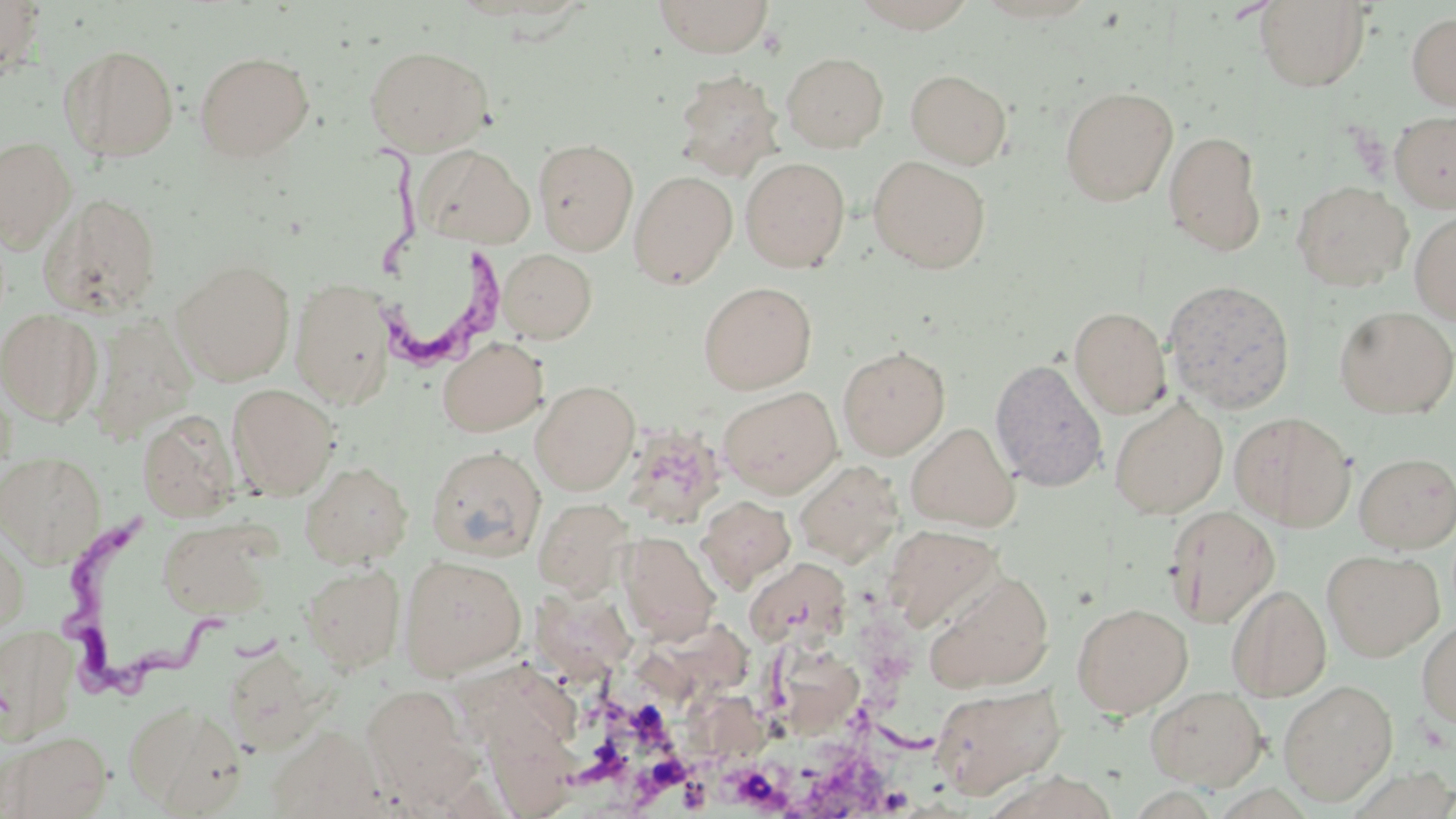
Summary:
  - Coordinate format: approximate bounding boxes as named x1/y1/x2/y2 corners in pixels
  - Uninfected red blood cell locations: (x1=0, y1=0, x2=45, y2=80), (x1=653, y1=0, x2=774, y2=58), (x1=853, y1=0, x2=978, y2=32), (x1=1254, y1=1, x2=1371, y2=92), (x1=1406, y1=11, x2=1456, y2=112), (x1=60, y1=44, x2=180, y2=162), (x1=365, y1=45, x2=493, y2=156), (x1=194, y1=51, x2=314, y2=162), (x1=782, y1=52, x2=888, y2=152), (x1=905, y1=69, x2=1012, y2=169), (x1=673, y1=70, x2=783, y2=181), (x1=1060, y1=86, x2=1178, y2=206), (x1=1389, y1=109, x2=1456, y2=213), (x1=1163, y1=130, x2=1266, y2=255), (x1=0, y1=136, x2=76, y2=251), (x1=532, y1=137, x2=639, y2=255), (x1=414, y1=144, x2=536, y2=249), (x1=868, y1=155, x2=991, y2=273), (x1=740, y1=157, x2=850, y2=272), (x1=629, y1=170, x2=738, y2=288), (x1=1291, y1=180, x2=1413, y2=291), (x1=39, y1=192, x2=164, y2=318), (x1=1410, y1=211, x2=1456, y2=325), (x1=497, y1=248, x2=597, y2=342), (x1=172, y1=260, x2=295, y2=385), (x1=290, y1=278, x2=395, y2=408), (x1=1162, y1=279, x2=1296, y2=413), (x1=698, y1=281, x2=817, y2=393), (x1=1069, y1=306, x2=1172, y2=419), (x1=1333, y1=306, x2=1456, y2=418), (x1=0, y1=308, x2=102, y2=425), (x1=88, y1=312, x2=198, y2=443), (x1=438, y1=337, x2=547, y2=437), (x1=837, y1=345, x2=951, y2=460), (x1=989, y1=358, x2=1107, y2=491), (x1=530, y1=380, x2=640, y2=495), (x1=227, y1=384, x2=339, y2=499), (x1=719, y1=386, x2=842, y2=499), (x1=1110, y1=398, x2=1228, y2=519), (x1=137, y1=410, x2=239, y2=522), (x1=1229, y1=411, x2=1356, y2=531), (x1=622, y1=421, x2=728, y2=530), (x1=906, y1=422, x2=1019, y2=531), (x1=426, y1=446, x2=546, y2=562), (x1=0, y1=452, x2=106, y2=567), (x1=1355, y1=452, x2=1456, y2=552), (x1=794, y1=459, x2=904, y2=566), (x1=301, y1=462, x2=412, y2=568), (x1=696, y1=496, x2=796, y2=591), (x1=532, y1=498, x2=633, y2=598), (x1=1165, y1=505, x2=1281, y2=628), (x1=158, y1=520, x2=274, y2=619), (x1=883, y1=524, x2=1005, y2=632), (x1=0, y1=526, x2=30, y2=638), (x1=618, y1=531, x2=720, y2=643), (x1=1322, y1=548, x2=1443, y2=661), (x1=399, y1=555, x2=527, y2=679), (x1=744, y1=557, x2=851, y2=650), (x1=300, y1=563, x2=406, y2=673), (x1=924, y1=570, x2=1056, y2=693), (x1=1227, y1=584, x2=1331, y2=702), (x1=530, y1=588, x2=642, y2=694), (x1=1071, y1=602, x2=1192, y2=718), (x1=1416, y1=618, x2=1456, y2=727), (x1=0, y1=624, x2=80, y2=746), (x1=1278, y1=679, x2=1399, y2=806), (x1=929, y1=683, x2=1067, y2=799), (x1=361, y1=684, x2=473, y2=800), (x1=1145, y1=685, x2=1268, y2=790), (x1=123, y1=700, x2=247, y2=815), (x1=481, y1=711, x2=583, y2=819), (x1=266, y1=725, x2=386, y2=818), (x1=2, y1=730, x2=112, y2=819)
  - Trypanosoma brucei locations: (x1=363, y1=131, x2=517, y2=376), (x1=56, y1=510, x2=232, y2=699)
  - Slide-level diagnosis: Trypanosoma brucei
  - Image size: 1456×819 pixels
  - Modality: optical microscopy
  - Field of view: single
  - Stain: May-Grünwald-Giemsa
  - Preparation: thin blood film
  - Magnification: 1000x